Assess this cell for malaria.
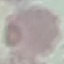
Uninfected.

capture = smartphone through the microscope eyepiece
stain = Giemsa
image type = automatically extracted cell patch, resized to 64 × 64 pixels
preparation = thin blood smear